Report the malaria status of this cell.
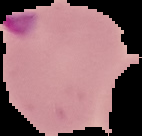
It is parasitized.

Summary:
  - Image type: segmented cell region on a black background
  - Preparation: thin blood film
  - Image size: 142×136 pixels